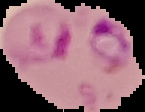

Summary:
  - Preparation: thin blood film
  - Malaria status: parasitized
  - Image size: 145×112 pixels
  - Image type: cell region segmented out of the field of view; surrounding area masked to black